Assess this cell for malaria.
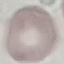

It is uninfected.

{
  "image_type": "automatically extracted cell patch, resized to 64 × 64 pixels",
  "stain": "Giemsa",
  "capture": "smartphone through the microscope eyepiece",
  "preparation": "thin blood smear"
}